Describe the morphology of the erythrocytes.
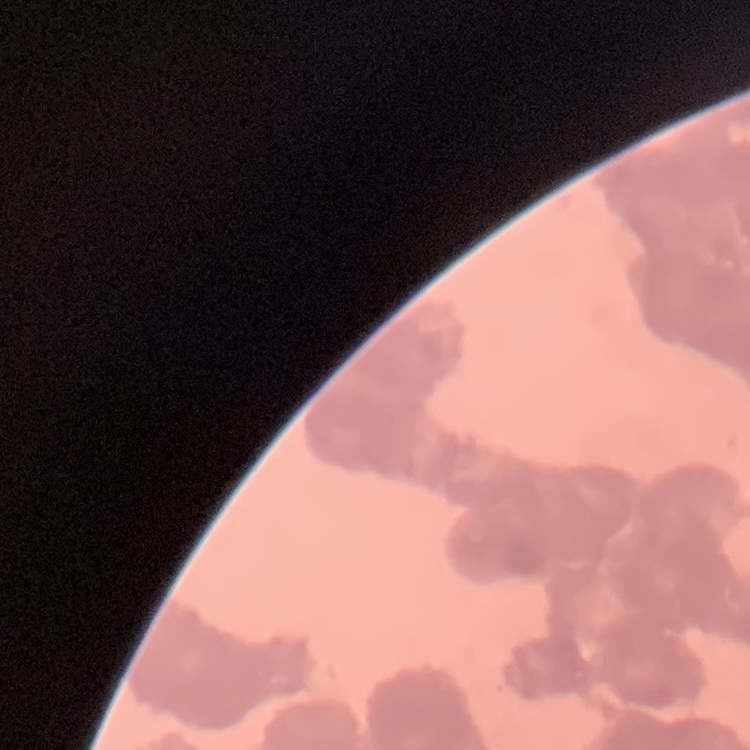

Rouleaux formation.

{
  "preparation": "thin blood smear",
  "image_type": "one tile cut from a larger photomicrograph",
  "stain": "Field's or Giemsa"
}